Assess this cell for malaria.
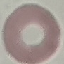
It is uninfected.

Automatically extracted cell patch, resized to 64 × 64 pixels. Giemsa stain. Thin blood smear. Photographed with a smartphone camera at the microscope eyepiece.